Classify the preparation.
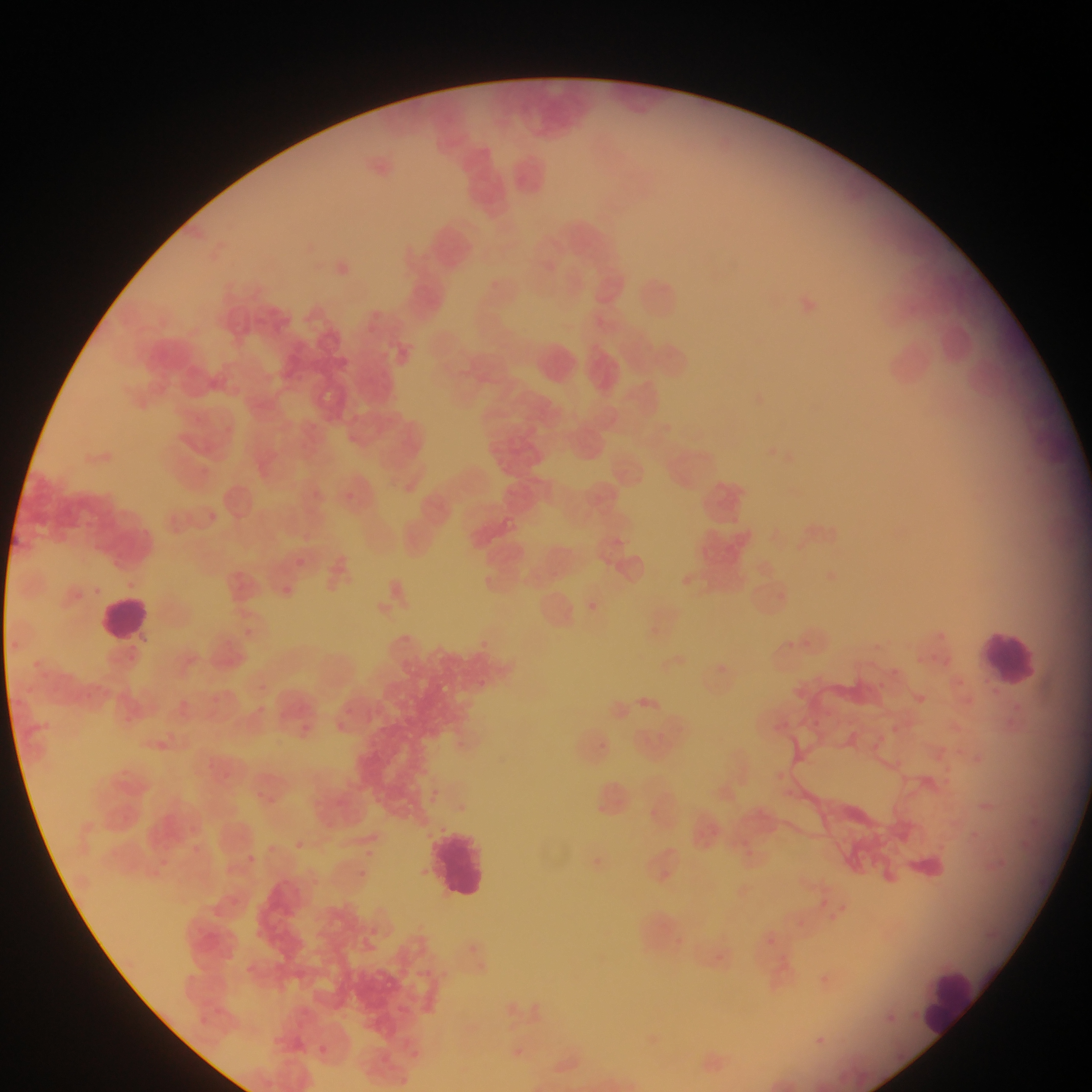
This is a thin smear.

Approximate bounding boxes as (left, top, right, bottom) in pixels.
Summary:
  - Malaria parasite locations: (208, 512, 217, 521), (295, 558, 304, 566), (282, 585, 293, 594) | approximate (x, y) pixel centers of objects too small to bound: (298, 376), (317, 494), (351, 496)
  - Leukocyte locations: (94, 591, 159, 646), (969, 618, 1044, 687), (430, 827, 491, 900), (923, 969, 979, 1034)
  - Country: Ghana
  - Field of view: single
  - Image size: 1092×1092 pixels
  - Capture: mobile-phone photograph through a microscope